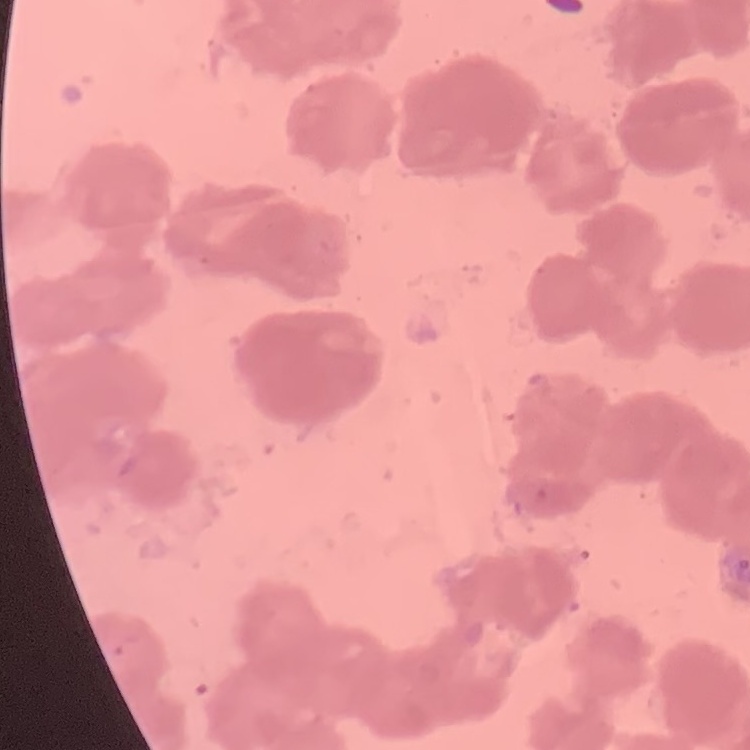 The erythrocytes exhibit rouleaux formation. Square crop of a larger photomicrograph. Field's or Giemsa stain. Thin blood film.